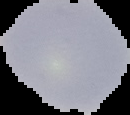
Summary:
  - Preparation: thin blood film
  - Image type: segmented cell region with the area outside set to black
  - Image size: 130×115 pixels
  - Result: no malaria parasites detected